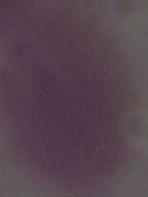

Summary:
  - Magnification: 1000x
  - Modality: micrograph
  - Identification: erythrocyte